Point out malaria parasites and leukocytes.
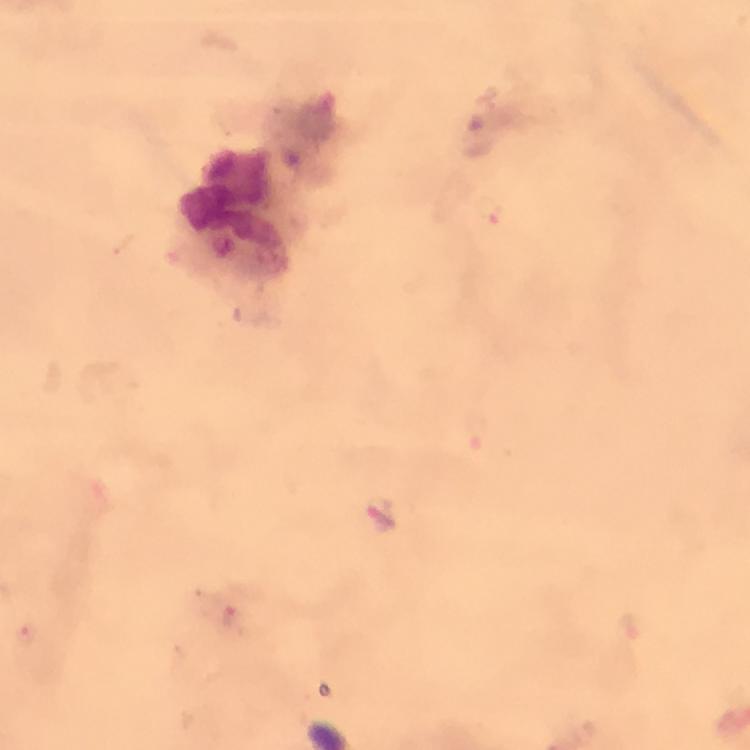
Approximate centers as [x, y] in pixels.
Malaria parasites: [491, 209], [380, 516], [233, 619], [631, 626], [31, 635].
Leukocytes: [232, 202].

From a malaria diagnostic workup. 100x magnification. Photographed through the microscope with a smartphone camera. Immersion oil applied. Thick smear. A crop from one field of view. Giemsa-stained preparation. Image is 750×750 pixels.